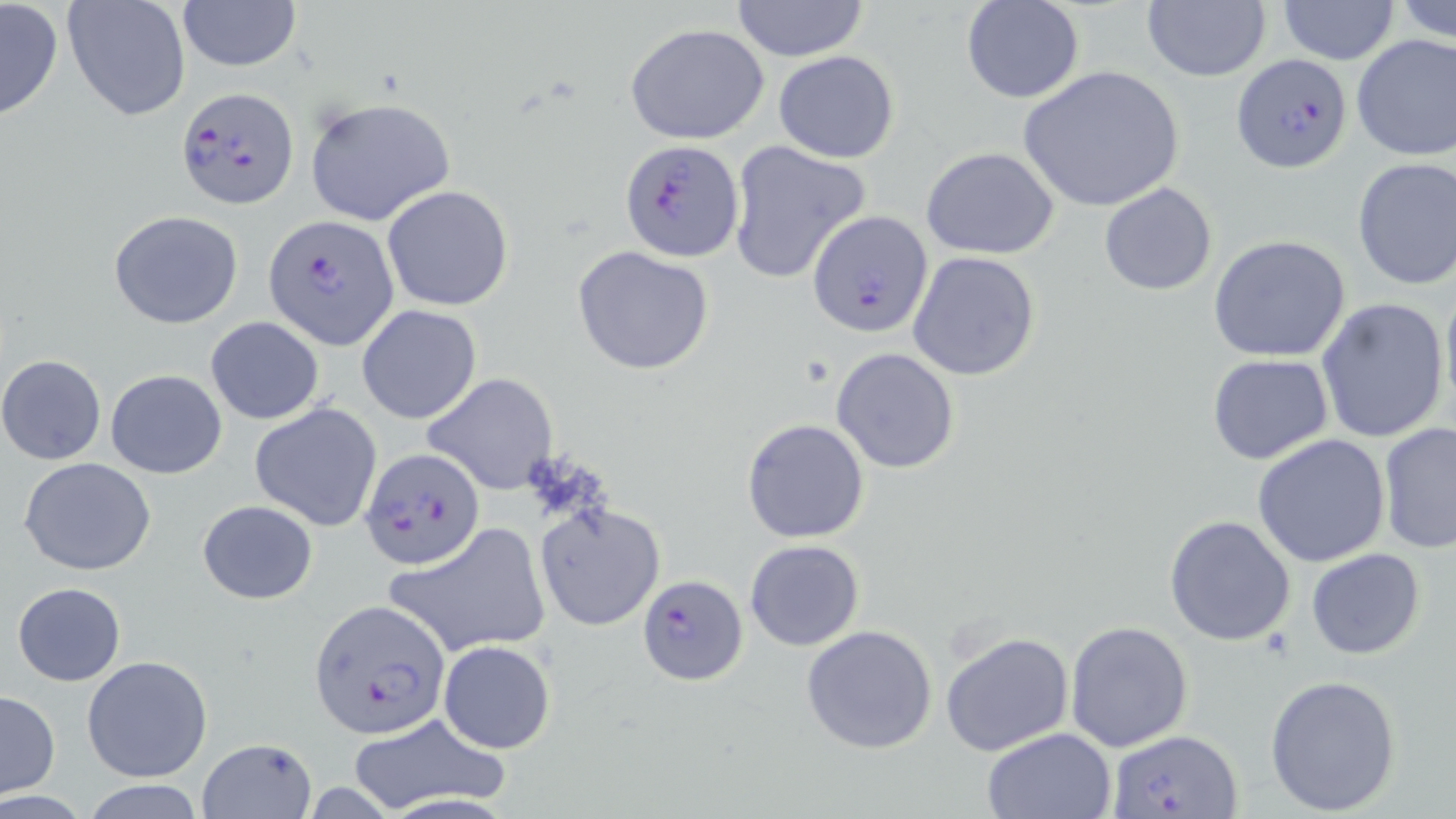
Summary:
  - Coordinate format: approximate bounding boxes as named x1/y1/x2/y2 corners in pixels
  - Uninfected red blood cell locations: (x1=0, y1=0, x2=65, y2=123), (x1=63, y1=0, x2=191, y2=123), (x1=177, y1=0, x2=302, y2=71), (x1=731, y1=0, x2=870, y2=60), (x1=962, y1=0, x2=1084, y2=103), (x1=1396, y1=0, x2=1456, y2=44), (x1=1140, y1=1, x2=1272, y2=82), (x1=1278, y1=1, x2=1400, y2=65), (x1=625, y1=22, x2=770, y2=145), (x1=1351, y1=33, x2=1456, y2=161), (x1=774, y1=50, x2=900, y2=163), (x1=1018, y1=65, x2=1184, y2=213), (x1=304, y1=96, x2=459, y2=227), (x1=726, y1=140, x2=873, y2=286), (x1=920, y1=147, x2=1061, y2=259), (x1=1352, y1=157, x2=1456, y2=290), (x1=1099, y1=182, x2=1217, y2=296), (x1=380, y1=185, x2=514, y2=312), (x1=109, y1=209, x2=244, y2=329), (x1=1208, y1=234, x2=1352, y2=362), (x1=572, y1=246, x2=715, y2=376), (x1=907, y1=252, x2=1041, y2=381), (x1=1439, y1=278, x2=1456, y2=418), (x1=1316, y1=297, x2=1451, y2=443), (x1=357, y1=305, x2=483, y2=424), (x1=205, y1=317, x2=325, y2=424), (x1=832, y1=347, x2=961, y2=473), (x1=1206, y1=353, x2=1334, y2=465), (x1=0, y1=354, x2=106, y2=464), (x1=105, y1=368, x2=227, y2=479), (x1=423, y1=373, x2=558, y2=494), (x1=249, y1=402, x2=384, y2=532), (x1=741, y1=418, x2=870, y2=543), (x1=1377, y1=422, x2=1456, y2=555), (x1=1251, y1=433, x2=1391, y2=568), (x1=18, y1=456, x2=157, y2=575), (x1=198, y1=499, x2=318, y2=604), (x1=535, y1=504, x2=666, y2=632), (x1=1164, y1=514, x2=1298, y2=647), (x1=386, y1=523, x2=551, y2=658), (x1=744, y1=539, x2=864, y2=651), (x1=1306, y1=548, x2=1428, y2=660), (x1=12, y1=582, x2=127, y2=685), (x1=1065, y1=621, x2=1194, y2=754), (x1=802, y1=625, x2=938, y2=755), (x1=939, y1=630, x2=1075, y2=756), (x1=438, y1=640, x2=557, y2=753), (x1=82, y1=655, x2=213, y2=783), (x1=1265, y1=674, x2=1402, y2=816), (x1=0, y1=691, x2=61, y2=796), (x1=345, y1=713, x2=511, y2=817), (x1=980, y1=726, x2=1117, y2=818), (x1=198, y1=737, x2=317, y2=819), (x1=79, y1=779, x2=209, y2=817)
  - Plasmodium falciparum-infected red blood cell locations: (x1=1234, y1=53, x2=1354, y2=171), (x1=176, y1=86, x2=297, y2=208), (x1=621, y1=141, x2=743, y2=262), (x1=808, y1=213, x2=931, y2=338), (x1=266, y1=214, x2=399, y2=349), (x1=361, y1=448, x2=487, y2=569), (x1=636, y1=575, x2=747, y2=685), (x1=310, y1=601, x2=450, y2=738), (x1=1108, y1=730, x2=1242, y2=819)
  - Slide-level diagnosis: Plasmodium falciparum
  - Stain: May-Grünwald-Giemsa
  - Image size: 1456×819 pixels
  - Magnification: 1000x
  - Preparation: thin blood film
  - Modality: light microscopy
  - Field of view: single